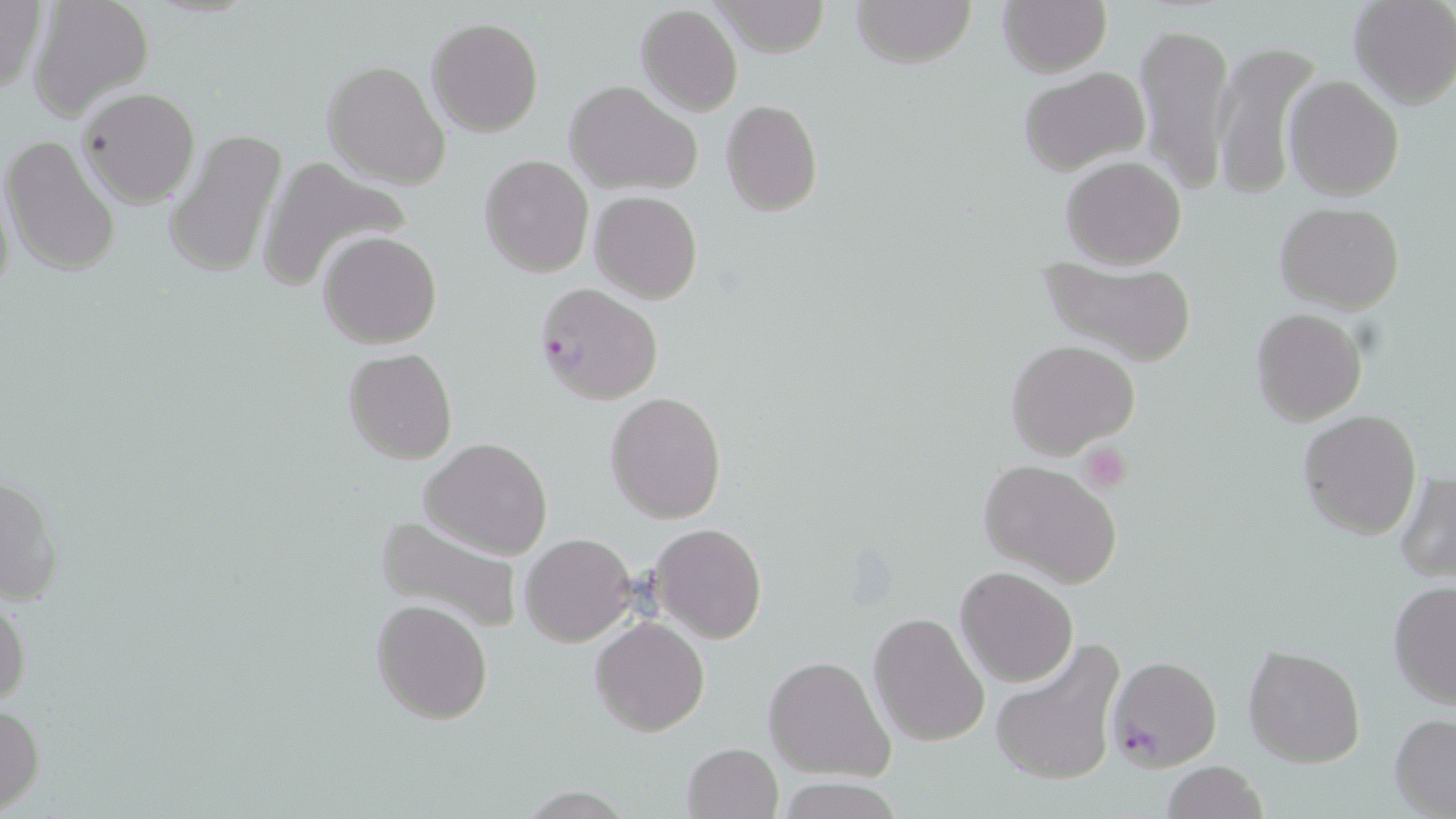
Summary:
  - Coordinate format: approximate bounding boxes as named x1/y1/x2/y2 corners in pixels
  - Uninfected red blood cell locations: (x1=0, y1=0, x2=48, y2=98), (x1=851, y1=0, x2=977, y2=70), (x1=998, y1=0, x2=1111, y2=76), (x1=1348, y1=0, x2=1456, y2=110), (x1=711, y1=1, x2=830, y2=56), (x1=28, y1=2, x2=151, y2=118), (x1=635, y1=4, x2=743, y2=117), (x1=427, y1=16, x2=543, y2=137), (x1=1135, y1=19, x2=1234, y2=198), (x1=1211, y1=39, x2=1321, y2=201), (x1=322, y1=60, x2=451, y2=189), (x1=1019, y1=67, x2=1151, y2=174), (x1=1283, y1=75, x2=1404, y2=201), (x1=565, y1=81, x2=700, y2=196), (x1=76, y1=88, x2=201, y2=208), (x1=720, y1=100, x2=823, y2=218), (x1=161, y1=127, x2=288, y2=278), (x1=1, y1=135, x2=121, y2=277), (x1=479, y1=154, x2=593, y2=277), (x1=1060, y1=154, x2=1188, y2=268), (x1=257, y1=155, x2=409, y2=291), (x1=589, y1=190, x2=704, y2=305), (x1=1274, y1=201, x2=1405, y2=314), (x1=572, y1=212, x2=690, y2=382), (x1=318, y1=230, x2=441, y2=349), (x1=1036, y1=256, x2=1197, y2=366), (x1=1250, y1=309, x2=1368, y2=428), (x1=1006, y1=339, x2=1141, y2=461), (x1=342, y1=346, x2=457, y2=465), (x1=604, y1=392, x2=727, y2=523), (x1=1298, y1=408, x2=1422, y2=542), (x1=419, y1=436, x2=553, y2=560), (x1=977, y1=457, x2=1124, y2=589), (x1=1, y1=470, x2=63, y2=608), (x1=1394, y1=472, x2=1455, y2=585), (x1=376, y1=513, x2=524, y2=638), (x1=650, y1=523, x2=767, y2=644), (x1=520, y1=533, x2=637, y2=646), (x1=954, y1=565, x2=1078, y2=687), (x1=1387, y1=580, x2=1455, y2=710), (x1=0, y1=588, x2=29, y2=711), (x1=371, y1=598, x2=494, y2=726), (x1=868, y1=612, x2=990, y2=748), (x1=590, y1=616, x2=710, y2=736), (x1=991, y1=639, x2=1124, y2=788), (x1=1242, y1=644, x2=1366, y2=768), (x1=764, y1=655, x2=895, y2=780), (x1=0, y1=702, x2=45, y2=815), (x1=1390, y1=713, x2=1456, y2=816), (x1=681, y1=743, x2=783, y2=819), (x1=1159, y1=760, x2=1269, y2=819)
  - Plasmodium falciparum-infected red blood cell locations: (x1=535, y1=282, x2=663, y2=405), (x1=1103, y1=652, x2=1223, y2=773)
  - Platelet locations: (x1=1081, y1=442, x2=1132, y2=491)
  - Slide-level diagnosis: Plasmodium falciparum
  - Image size: 1456×819 pixels
  - Field of view: single
  - Magnification: 1000x
  - Stain: May-Grünwald-Giemsa
  - Preparation: thin blood film
  - Modality: optical microscopy